Locate and identify every blood parasite.
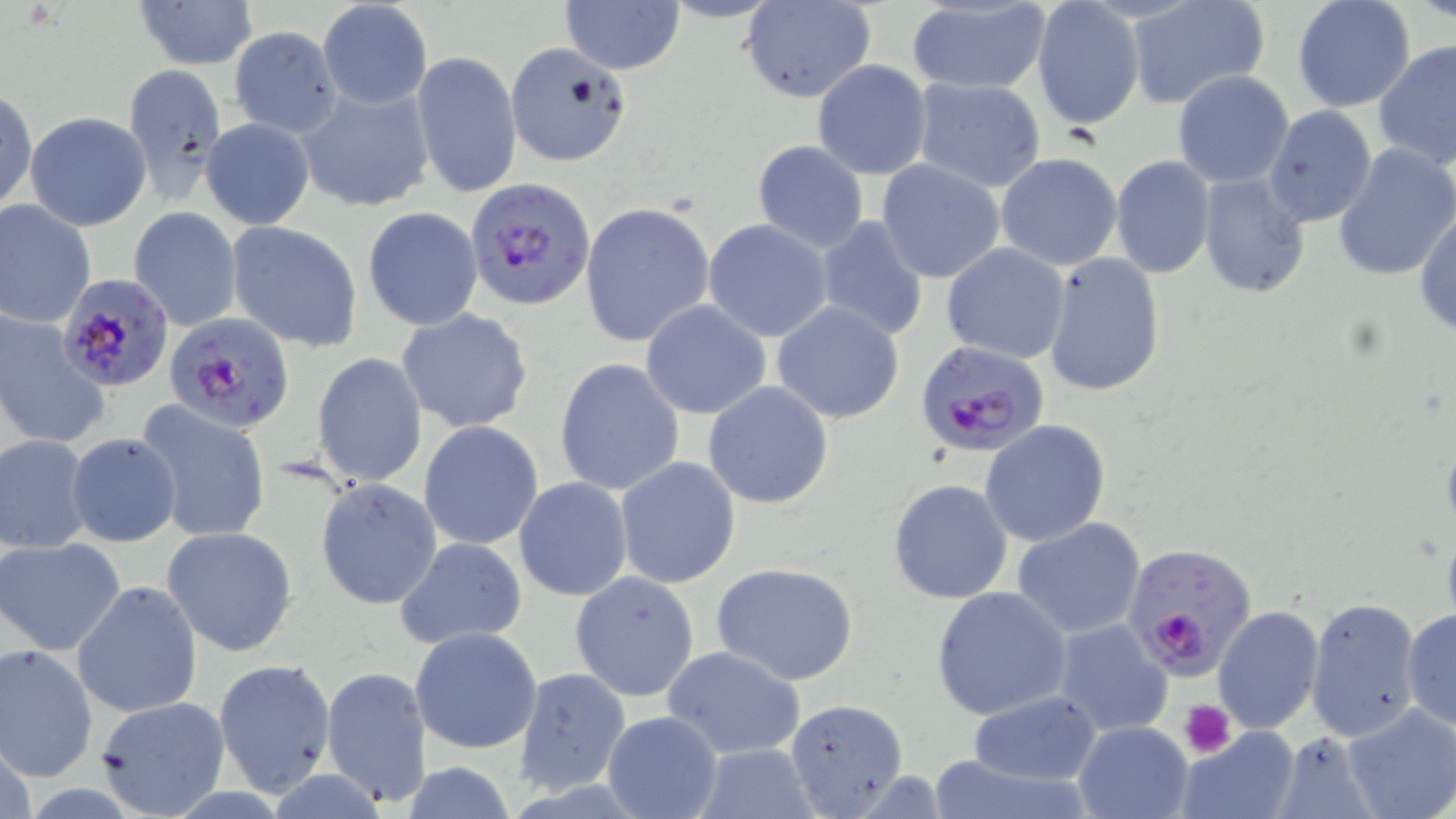
Approximate bounding boxes as named x1/y1/x2/y2 corners in pixels.
Plasmodium falciparum-infected red blood cells: (x1=468, y1=178, x2=597, y2=310), (x1=58, y1=271, x2=176, y2=391), (x1=166, y1=311, x2=293, y2=430), (x1=915, y1=338, x2=1047, y2=459), (x1=1133, y1=550, x2=1266, y2=687).
No Plasmodium ovale, Plasmodium malariae, Plasmodium vivax, Babesia divergens, or Trypanosoma brucei observed.

Summary:
  - Platelet locations: (x1=1181, y1=702, x2=1234, y2=757)
  - Uninfected red blood cell locations: (x1=132, y1=0, x2=258, y2=72), (x1=317, y1=0, x2=433, y2=108), (x1=560, y1=0, x2=686, y2=74), (x1=741, y1=0, x2=877, y2=103), (x1=1126, y1=0, x2=1271, y2=111), (x1=1292, y1=0, x2=1417, y2=113), (x1=1031, y1=2, x2=1145, y2=131), (x1=904, y1=3, x2=1052, y2=95), (x1=228, y1=27, x2=342, y2=136), (x1=1373, y1=40, x2=1456, y2=171), (x1=505, y1=41, x2=635, y2=168), (x1=411, y1=50, x2=521, y2=200), (x1=811, y1=61, x2=932, y2=179), (x1=122, y1=64, x2=225, y2=199), (x1=1171, y1=71, x2=1295, y2=189), (x1=910, y1=77, x2=1047, y2=193), (x1=299, y1=85, x2=435, y2=213), (x1=1, y1=87, x2=37, y2=215), (x1=1263, y1=105, x2=1377, y2=226), (x1=26, y1=111, x2=150, y2=231), (x1=202, y1=118, x2=314, y2=231), (x1=751, y1=140, x2=869, y2=253), (x1=1332, y1=143, x2=1456, y2=284), (x1=995, y1=153, x2=1122, y2=272), (x1=1110, y1=154, x2=1215, y2=279), (x1=876, y1=159, x2=1005, y2=283), (x1=1198, y1=173, x2=1313, y2=297), (x1=0, y1=199, x2=96, y2=327), (x1=579, y1=201, x2=715, y2=347), (x1=1414, y1=205, x2=1456, y2=337), (x1=129, y1=206, x2=243, y2=331), (x1=362, y1=207, x2=484, y2=332), (x1=815, y1=218, x2=929, y2=343), (x1=703, y1=219, x2=834, y2=342), (x1=227, y1=222, x2=363, y2=351), (x1=941, y1=241, x2=1071, y2=364), (x1=1041, y1=250, x2=1167, y2=396), (x1=640, y1=300, x2=771, y2=419), (x1=771, y1=301, x2=905, y2=424), (x1=396, y1=307, x2=534, y2=433), (x1=0, y1=313, x2=106, y2=452), (x1=314, y1=352, x2=428, y2=487), (x1=554, y1=357, x2=686, y2=498), (x1=702, y1=380, x2=834, y2=510), (x1=139, y1=403, x2=273, y2=542), (x1=979, y1=419, x2=1111, y2=547), (x1=419, y1=420, x2=543, y2=551), (x1=1, y1=432, x2=91, y2=553), (x1=66, y1=432, x2=182, y2=548), (x1=614, y1=456, x2=741, y2=589), (x1=515, y1=477, x2=634, y2=602), (x1=315, y1=478, x2=442, y2=611), (x1=888, y1=478, x2=1014, y2=605), (x1=1012, y1=517, x2=1147, y2=639), (x1=161, y1=526, x2=298, y2=656), (x1=0, y1=537, x2=126, y2=657), (x1=395, y1=537, x2=528, y2=651), (x1=712, y1=563, x2=859, y2=685), (x1=570, y1=571, x2=701, y2=702), (x1=71, y1=580, x2=203, y2=719), (x1=932, y1=586, x2=1072, y2=722), (x1=1307, y1=596, x2=1422, y2=742), (x1=1212, y1=606, x2=1324, y2=734), (x1=1402, y1=609, x2=1456, y2=731), (x1=1052, y1=619, x2=1174, y2=739), (x1=410, y1=627, x2=544, y2=754), (x1=0, y1=643, x2=99, y2=783), (x1=662, y1=646, x2=809, y2=762), (x1=214, y1=659, x2=337, y2=799), (x1=321, y1=665, x2=431, y2=809), (x1=514, y1=667, x2=631, y2=794), (x1=969, y1=691, x2=1102, y2=785), (x1=96, y1=695, x2=231, y2=816), (x1=783, y1=698, x2=909, y2=816), (x1=1341, y1=705, x2=1456, y2=819), (x1=602, y1=710, x2=723, y2=819), (x1=1073, y1=720, x2=1194, y2=818), (x1=1177, y1=724, x2=1302, y2=819), (x1=1272, y1=731, x2=1379, y2=819), (x1=691, y1=744, x2=820, y2=819), (x1=926, y1=752, x2=1089, y2=818), (x1=401, y1=762, x2=518, y2=818)
  - Slide-level diagnosis: Plasmodium falciparum
  - Stain: May-Grünwald-Giemsa
  - Field of view: one of a larger specimen
  - Preparation: thin blood film
  - Magnification: 1000x
  - Image size: 1456×819 pixels
  - Modality: optical microscopy